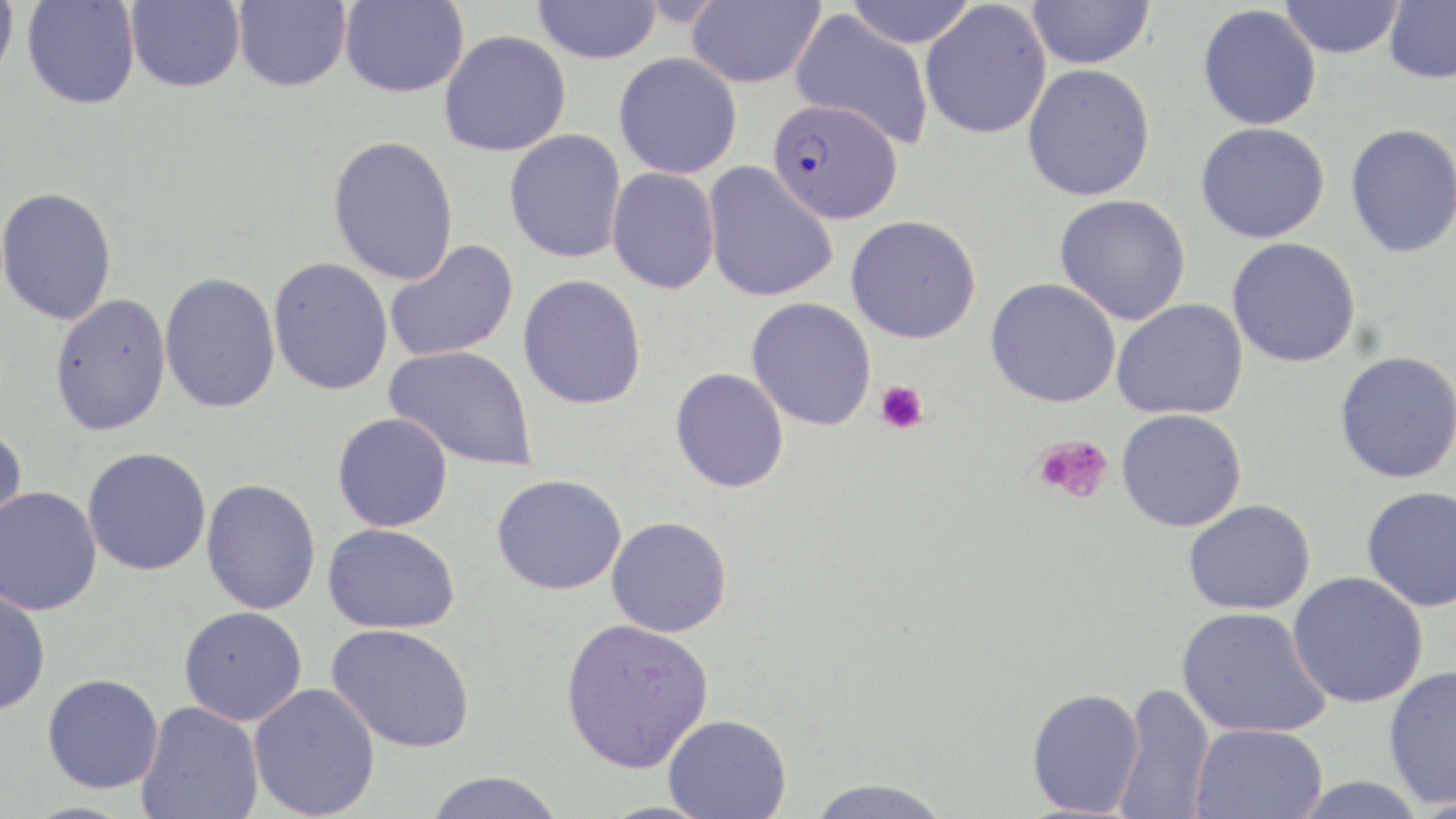
Approximate bounding boxes as (x1, y1, x2, y2) in pixels. Plasmodium falciparum-infected red blood cell locations: (768, 98, 903, 224). Platelet locations: (874, 380, 929, 434), (1034, 434, 1114, 505). Uninfected red blood cell locations: (125, 0, 245, 92), (340, 0, 469, 97), (686, 0, 826, 89), (843, 0, 979, 48), (1027, 0, 1155, 69), (0, 1, 19, 83), (22, 1, 140, 109), (233, 1, 351, 92), (532, 1, 663, 64), (920, 1, 1052, 139), (1280, 1, 1405, 59), (1384, 1, 1456, 84), (1197, 4, 1322, 131), (789, 8, 935, 150), (439, 30, 571, 156), (614, 53, 742, 179), (1022, 63, 1155, 201), (1196, 122, 1330, 243), (1345, 123, 1456, 258), (504, 129, 627, 263), (327, 135, 459, 285), (703, 162, 838, 303), (607, 167, 720, 294), (0, 186, 118, 326), (1055, 194, 1191, 325), (846, 214, 981, 343), (1227, 237, 1361, 368), (384, 240, 519, 363), (268, 257, 393, 395), (159, 272, 281, 413), (518, 274, 647, 409), (985, 278, 1121, 408), (50, 293, 171, 436), (746, 297, 877, 431), (1112, 299, 1248, 420), (384, 345, 539, 471), (1335, 351, 1456, 483), (671, 368, 789, 493), (1116, 409, 1247, 532), (332, 412, 453, 532), (0, 422, 28, 546), (83, 447, 211, 575), (492, 473, 627, 595), (201, 478, 321, 614), (1362, 485, 1456, 613), (0, 487, 102, 615), (1183, 499, 1316, 614), (606, 516, 732, 637), (323, 522, 460, 634), (1287, 571, 1429, 709), (0, 588, 51, 716), (179, 606, 307, 726), (1176, 606, 1331, 739), (560, 618, 714, 773), (327, 623, 475, 753), (1383, 665, 1456, 808), (42, 673, 164, 793), (248, 682, 381, 818), (1114, 683, 1216, 819), (1026, 687, 1145, 816), (136, 702, 264, 819), (663, 714, 791, 818), (1190, 723, 1328, 819), (423, 772, 566, 818), (1287, 776, 1431, 819), (804, 777, 954, 818). Slide-level diagnosis: Plasmodium falciparum. Optical microscopy. May-Grünwald-Giemsa-stained preparation. 1000x magnification. One field of a larger specimen. Image is 1456×819 pixels. Thin blood smear.